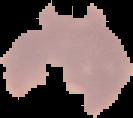

Summary:
  - Result: Plasmodium parasites identified
  - Preparation: thin blood film
  - Image size: 133×118 pixels
  - Image type: segmented cell region on a black background